Outline each blood parasite and name the species.
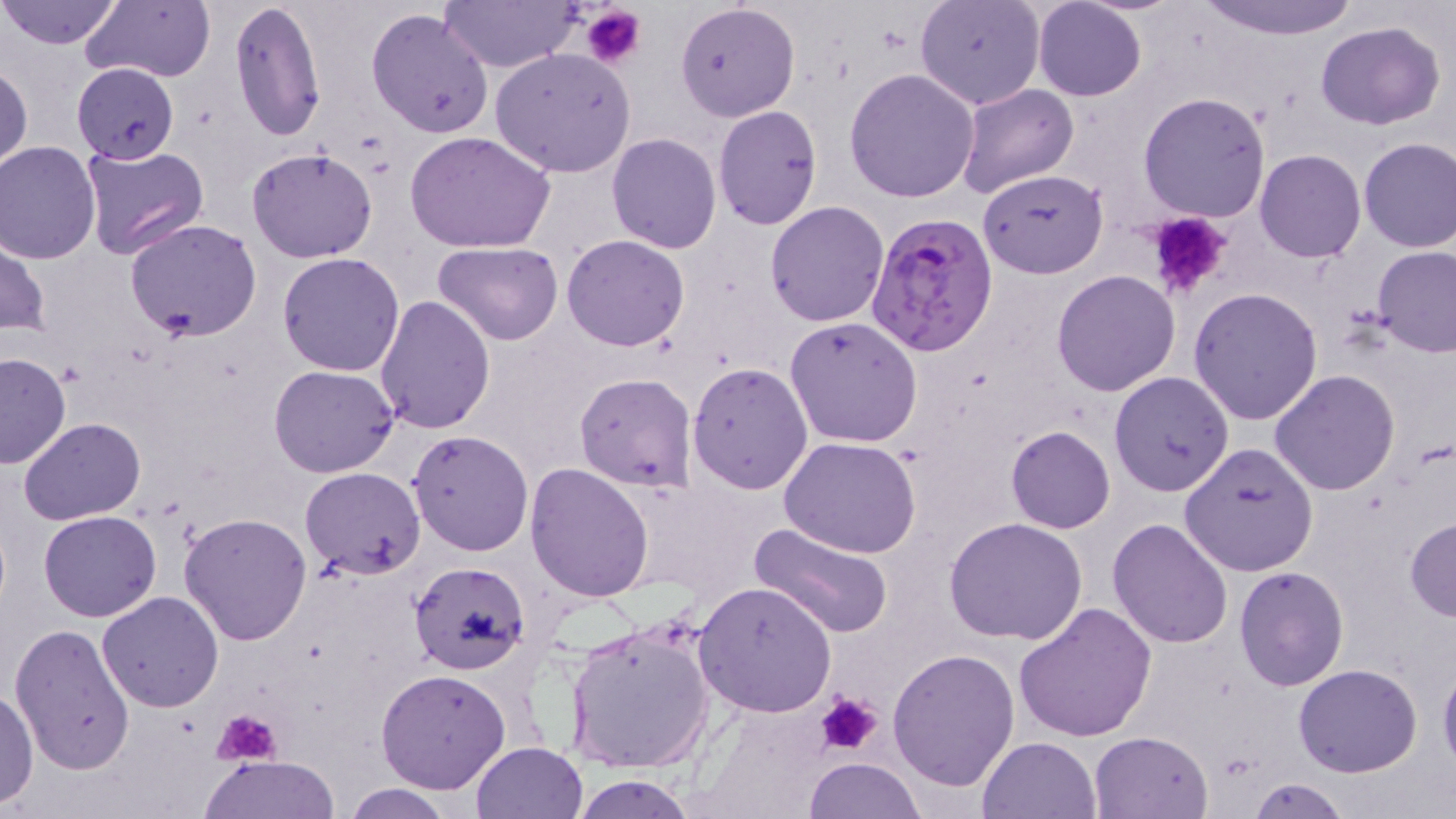
Approximate bounding boxes as named x1/y1/x2/y2 corners in pixels.
Plasmodium falciparum-infected red blood cells: (x1=865, y1=213, x2=998, y2=358).
No Plasmodium ovale, Plasmodium malariae, Plasmodium vivax, Babesia divergens, or Trypanosoma brucei observed.

Summary:
  - Uninfected red blood cell locations: (x1=0, y1=0, x2=121, y2=49), (x1=229, y1=0, x2=326, y2=142), (x1=437, y1=0, x2=580, y2=73), (x1=915, y1=0, x2=1045, y2=110), (x1=1032, y1=0, x2=1147, y2=101), (x1=1193, y1=0, x2=1363, y2=41), (x1=80, y1=1, x2=216, y2=85), (x1=674, y1=2, x2=798, y2=122), (x1=366, y1=7, x2=495, y2=141), (x1=1315, y1=22, x2=1445, y2=131), (x1=489, y1=48, x2=637, y2=176), (x1=0, y1=58, x2=32, y2=175), (x1=72, y1=63, x2=179, y2=163), (x1=844, y1=69, x2=981, y2=202), (x1=955, y1=82, x2=1079, y2=200), (x1=1136, y1=91, x2=1271, y2=224), (x1=713, y1=104, x2=823, y2=231), (x1=406, y1=130, x2=556, y2=253), (x1=606, y1=133, x2=723, y2=254), (x1=1358, y1=138, x2=1456, y2=254), (x1=0, y1=142, x2=102, y2=262), (x1=78, y1=144, x2=208, y2=262), (x1=246, y1=146, x2=379, y2=263), (x1=1255, y1=148, x2=1366, y2=263), (x1=977, y1=170, x2=1108, y2=278), (x1=764, y1=200, x2=889, y2=327), (x1=124, y1=217, x2=264, y2=340), (x1=0, y1=228, x2=47, y2=339), (x1=562, y1=234, x2=690, y2=351), (x1=433, y1=241, x2=564, y2=346), (x1=1374, y1=247, x2=1456, y2=358), (x1=278, y1=253, x2=405, y2=376), (x1=1052, y1=269, x2=1180, y2=396), (x1=1188, y1=288, x2=1324, y2=425), (x1=373, y1=294, x2=495, y2=435), (x1=783, y1=317, x2=923, y2=449), (x1=1, y1=352, x2=70, y2=467), (x1=687, y1=363, x2=813, y2=495), (x1=269, y1=365, x2=400, y2=477), (x1=1270, y1=370, x2=1400, y2=495), (x1=1109, y1=371, x2=1234, y2=496), (x1=574, y1=373, x2=698, y2=492), (x1=18, y1=418, x2=145, y2=525), (x1=1006, y1=425, x2=1114, y2=533), (x1=407, y1=429, x2=533, y2=557), (x1=779, y1=436, x2=922, y2=557), (x1=1179, y1=442, x2=1319, y2=576), (x1=524, y1=463, x2=654, y2=601), (x1=300, y1=467, x2=427, y2=580), (x1=39, y1=510, x2=162, y2=621), (x1=179, y1=514, x2=313, y2=645), (x1=1107, y1=517, x2=1235, y2=649), (x1=1405, y1=517, x2=1456, y2=622), (x1=946, y1=518, x2=1088, y2=645), (x1=749, y1=523, x2=896, y2=641), (x1=408, y1=560, x2=530, y2=676), (x1=1234, y1=566, x2=1349, y2=690), (x1=694, y1=582, x2=837, y2=717), (x1=97, y1=591, x2=225, y2=712), (x1=1012, y1=601, x2=1155, y2=742), (x1=562, y1=616, x2=717, y2=776), (x1=9, y1=623, x2=137, y2=776), (x1=887, y1=648, x2=1019, y2=790), (x1=1438, y1=658, x2=1456, y2=774), (x1=1293, y1=663, x2=1422, y2=776), (x1=376, y1=668, x2=511, y2=794), (x1=1, y1=688, x2=39, y2=808), (x1=1089, y1=731, x2=1212, y2=817), (x1=978, y1=736, x2=1101, y2=819), (x1=470, y1=741, x2=588, y2=819), (x1=201, y1=754, x2=340, y2=818), (x1=804, y1=757, x2=927, y2=818), (x1=567, y1=773, x2=701, y2=818), (x1=1245, y1=778, x2=1352, y2=818), (x1=342, y1=783, x2=459, y2=818)
  - Platelet locations: (x1=582, y1=5, x2=644, y2=69), (x1=1142, y1=211, x2=1234, y2=300), (x1=817, y1=691, x2=882, y2=754), (x1=213, y1=707, x2=282, y2=767)
  - Slide-level diagnosis: Plasmodium falciparum
  - Modality: optical microscopy
  - Magnification: 1000x
  - Image size: 1456×819 pixels
  - Preparation: thin blood smear
  - Stain: May-Grünwald-Giemsa
  - Field of view: single